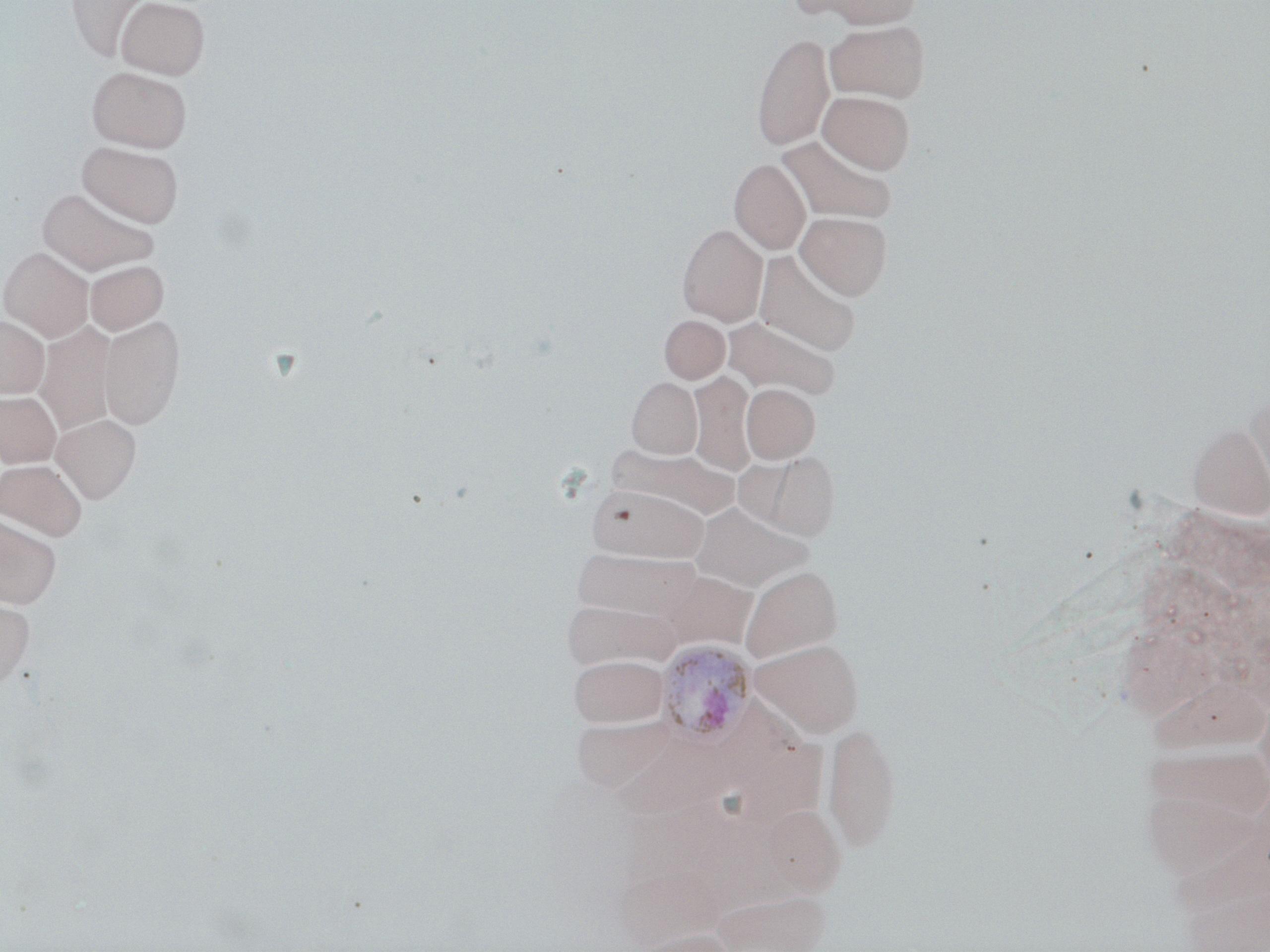 Approximate bounding boxes as (x1, y1, x2, y2) in pixels. Uninfected red blood cell locations: (66, 0, 154, 60), (116, 0, 209, 78), (809, 0, 920, 28), (825, 20, 930, 102), (751, 33, 835, 150), (87, 66, 191, 152), (818, 90, 915, 173), (777, 134, 898, 224), (77, 141, 184, 227), (729, 158, 811, 254), (37, 187, 158, 275), (796, 211, 892, 299), (677, 223, 767, 325), (0, 247, 94, 342), (754, 250, 861, 356), (85, 260, 168, 335), (100, 315, 185, 430), (659, 315, 730, 383), (0, 316, 49, 397), (723, 317, 840, 400), (34, 322, 116, 435), (688, 371, 756, 477), (627, 377, 703, 458), (741, 383, 820, 463), (0, 390, 62, 467), (1246, 395, 1270, 503), (52, 414, 141, 503), (1188, 423, 1270, 521), (605, 443, 738, 521), (753, 451, 839, 539), (0, 459, 87, 541), (587, 484, 708, 563), (691, 503, 810, 592), (0, 515, 61, 609), (572, 548, 702, 623), (740, 565, 843, 662), (662, 570, 756, 650), (0, 598, 34, 691), (750, 639, 863, 736), (569, 654, 668, 726), (570, 712, 678, 792), (824, 720, 901, 852), (614, 737, 742, 819), (740, 740, 836, 823), (767, 806, 850, 903), (610, 867, 729, 945), (709, 888, 833, 952), (631, 929, 738, 952). Plasmodium ovale-infected red blood cell locations: (655, 639, 757, 744). Slide-level diagnosis: Plasmodium ovale. 1000x magnification. Image is 1270×952 pixels. Light microscopy. Thin blood film. One field of a larger specimen. May-Grünwald-Giemsa-stained preparation.